Assess this cell for malaria.
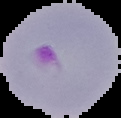
Parasitized.

Summary:
  - Image size: 121×118 pixels
  - Image type: cell region segmented out of the field of view; surrounding area masked to black
  - Preparation: thin blood film